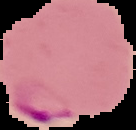 Result: malaria parasites detected. Image is 136×130 pixels. Cell region segmented out of the field of view; the surrounding area is masked to black. From a thin blood film.